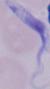

Summary:
  - Identification: trypanosome
  - Modality: micrograph
  - Magnification: 1000x